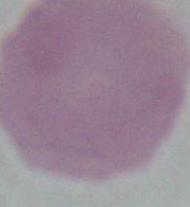
magnification = 1000x
identification = erythrocyte
modality = photomicrograph